Locate every uninfected red blood cell.
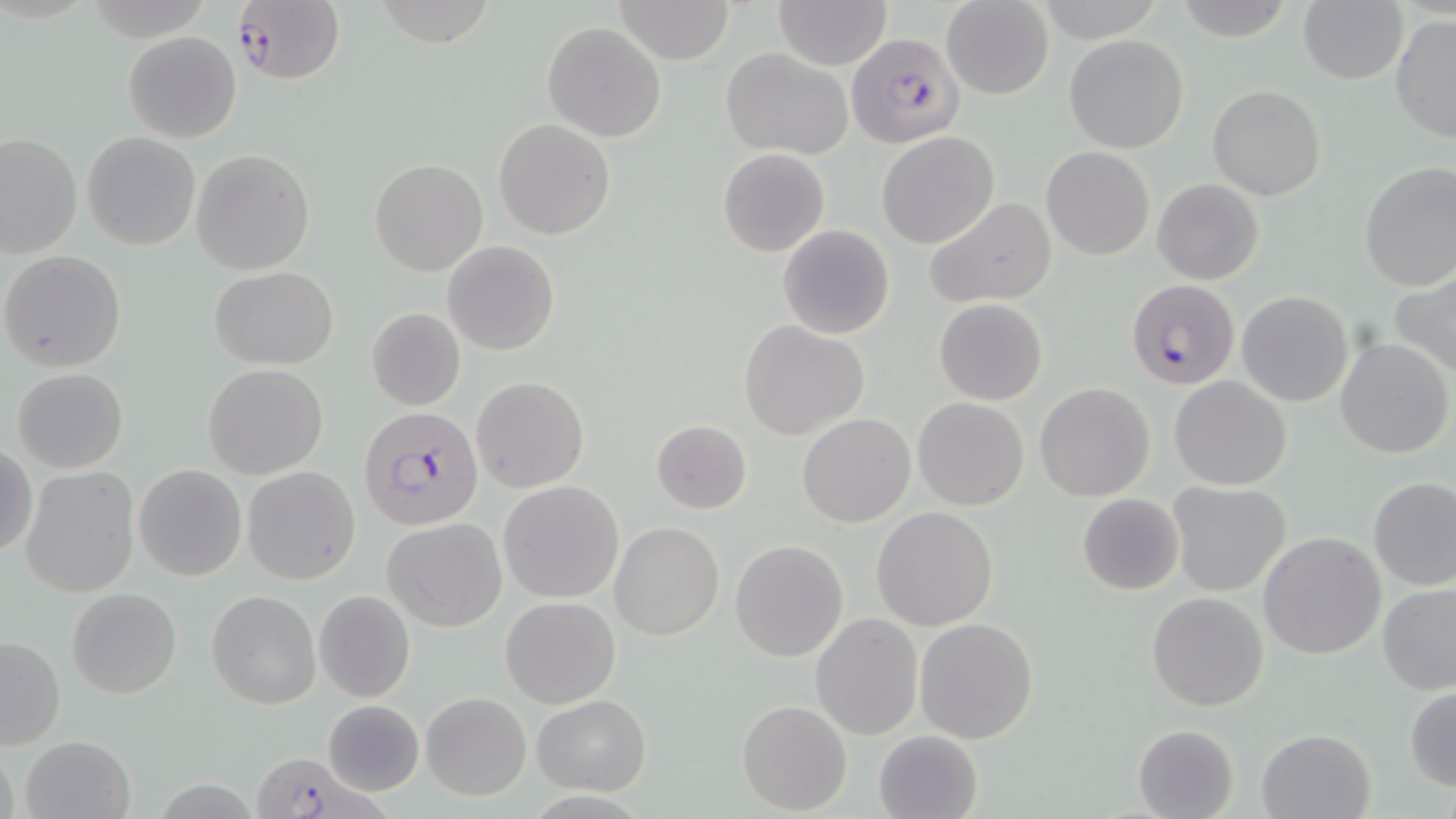
Approximate bounding boxes as [x1, y1, x2, y2] in pixels.
Uninfected red blood cells: [613, 0, 736, 64], [771, 0, 891, 70], [1299, 0, 1409, 85], [940, 1, 1054, 99], [1169, 2, 1295, 40], [1389, 13, 1456, 145], [542, 22, 667, 142], [123, 31, 242, 143], [1063, 34, 1188, 154], [722, 48, 853, 159], [1208, 85, 1326, 200], [494, 119, 615, 239], [878, 131, 1000, 249], [82, 132, 200, 250], [0, 133, 82, 259], [718, 147, 830, 256], [1042, 147, 1154, 261], [190, 149, 316, 274], [369, 158, 488, 276], [1358, 162, 1456, 291], [1152, 179, 1264, 286], [926, 197, 1056, 308], [776, 224, 896, 340], [443, 240, 560, 356], [1, 250, 127, 372], [211, 267, 337, 370], [1391, 269, 1456, 381], [1236, 290, 1355, 407], [933, 299, 1048, 405], [367, 308, 467, 411], [740, 321, 870, 440], [1336, 338, 1453, 459], [201, 363, 329, 478], [11, 368, 128, 474], [471, 376, 590, 493], [1170, 376, 1293, 491], [1033, 382, 1157, 501], [913, 397, 1029, 510], [798, 413, 916, 528], [650, 419, 753, 513], [1, 445, 37, 561], [134, 465, 248, 582], [19, 466, 140, 597], [242, 466, 360, 584], [1368, 475, 1456, 591], [499, 481, 623, 603], [1167, 482, 1293, 598], [1077, 492, 1184, 596], [871, 507, 999, 630], [382, 518, 507, 633], [610, 521, 724, 640], [1258, 532, 1387, 661], [730, 540, 848, 661], [1377, 583, 1456, 695], [66, 588, 182, 698], [313, 589, 416, 703], [206, 591, 321, 708], [1147, 592, 1268, 711], [501, 596, 620, 709], [810, 614, 923, 738], [915, 616, 1039, 743], [0, 632, 65, 750], [1404, 687, 1456, 792], [421, 691, 531, 801], [531, 694, 652, 796], [322, 699, 426, 796], [737, 700, 852, 815], [1133, 724, 1239, 818], [1255, 727, 1377, 819], [873, 729, 983, 818], [18, 733, 137, 819], [0, 738, 19, 819].

slide-level diagnosis = Plasmodium falciparum
stain = May-Grünwald-Giemsa
Plasmodium falciparum-infected red blood cell locations = approximate bounding boxes as [x1, y1, x2, y2] in pixels: [231, 0, 344, 86], [845, 33, 964, 150], [1126, 278, 1240, 390], [359, 407, 485, 530], [248, 751, 375, 818]
preparation = thin blood smear
magnification = 1000x
field of view = single
image size = 1456×819 pixels
modality = light microscopy